Locate every malaria parasite and identify its life-cycle stage.
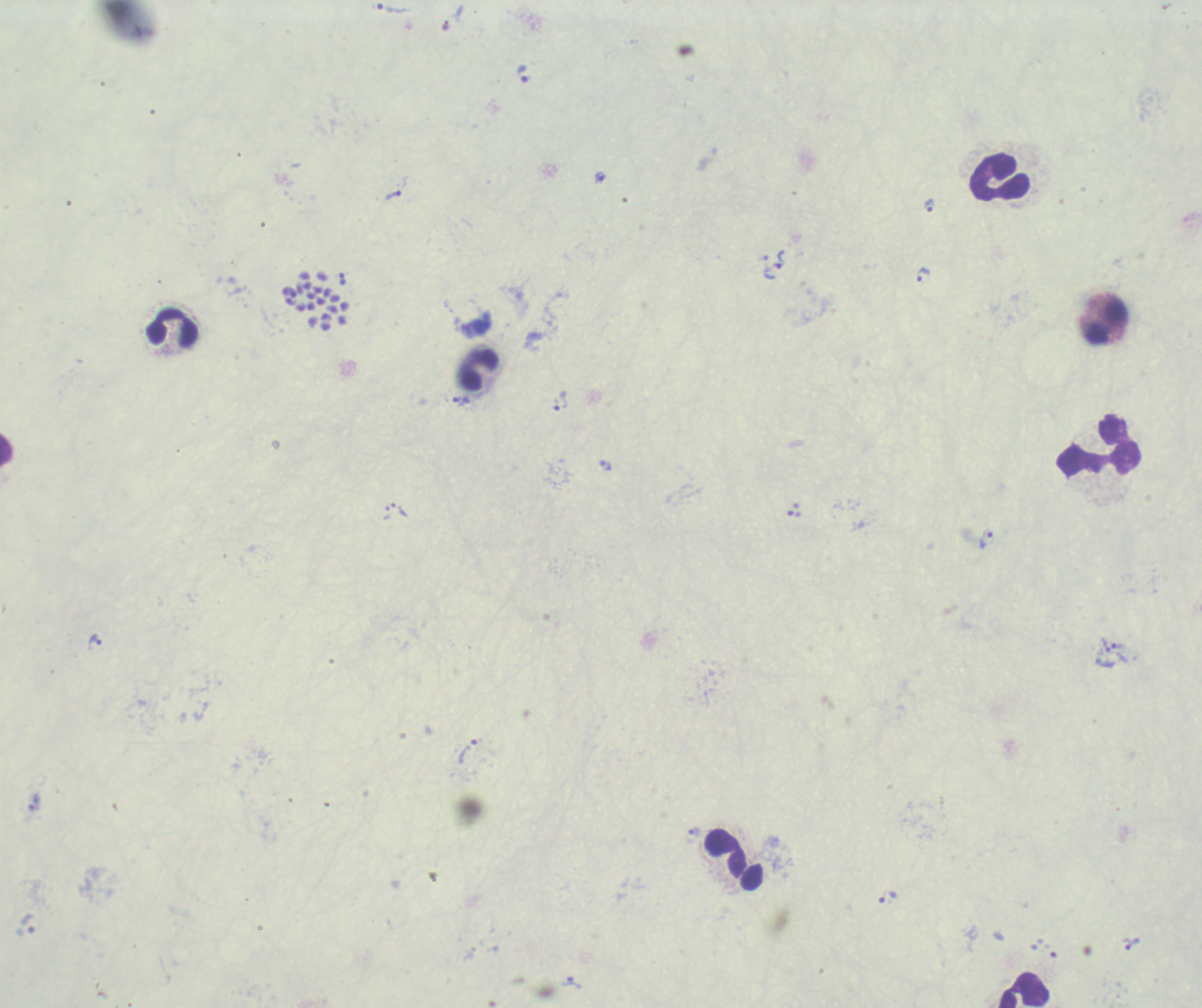

Approximate centers as [x, y] in pixels.
Trophozoites: [390, 7], [523, 74], [601, 178], [393, 195], [929, 205], [780, 259], [924, 275], [342, 280], [460, 400], [560, 400], [606, 465], [400, 511], [986, 538], [94, 641], [1106, 645], [1118, 646], [468, 751], [694, 832], [888, 897], [1130, 943], [572, 983].
Schizonts: [315, 308].
No gametocyte forms observed.

{
  "image_size": "1202×1008 pixels",
  "magnification": "100x",
  "leukocyte_locations": "approximate centers as [x, y] in pixels: [999, 177], [1107, 322], [174, 328], [479, 368], [1098, 444], [6, 450], [726, 854], [1024, 990]",
  "background_quality": "unsatisfactory",
  "preparation": "thick blood film",
  "stain": "Romanowsky",
  "field_of_view": "one from this slide",
  "context": "previously used in an actual diagnosis"
}